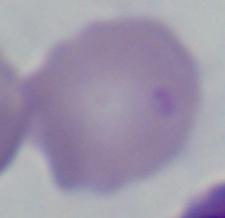

Summary:
  - Magnification: 1000x
  - Modality: micrograph
  - Identification: Babesia